Name the blood parasite species.
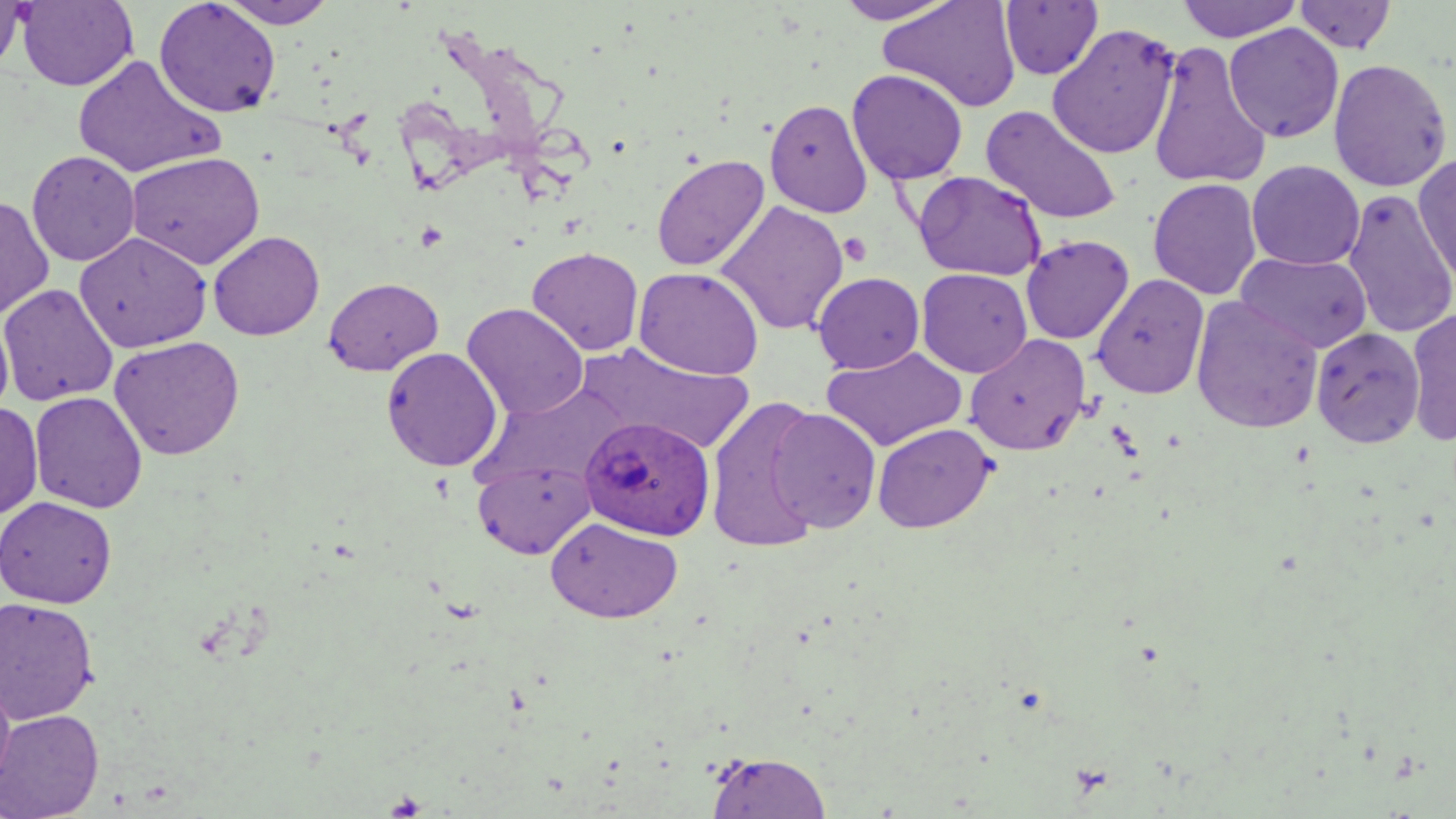
Plasmodium ovale.

Approximate bounding boxes as named x1/y1/x2/y2 corners in pixels. Platelet locations: (x1=415, y1=222, x2=448, y2=251), (x1=838, y1=233, x2=873, y2=266). Uninfected red blood cell locations: (x1=0, y1=0, x2=27, y2=76), (x1=16, y1=0, x2=138, y2=91), (x1=154, y1=0, x2=281, y2=118), (x1=217, y1=0, x2=338, y2=28), (x1=832, y1=0, x2=961, y2=25), (x1=879, y1=0, x2=1022, y2=112), (x1=1175, y1=0, x2=1304, y2=42), (x1=1000, y1=1, x2=1103, y2=80), (x1=1293, y1=1, x2=1398, y2=54), (x1=1046, y1=23, x2=1180, y2=160), (x1=1224, y1=23, x2=1344, y2=143), (x1=1149, y1=40, x2=1272, y2=191), (x1=72, y1=53, x2=225, y2=180), (x1=1328, y1=57, x2=1452, y2=192), (x1=847, y1=69, x2=968, y2=185), (x1=764, y1=99, x2=873, y2=218), (x1=980, y1=105, x2=1122, y2=226), (x1=26, y1=150, x2=141, y2=266), (x1=126, y1=151, x2=266, y2=270), (x1=1413, y1=152, x2=1456, y2=291), (x1=651, y1=153, x2=770, y2=272), (x1=1247, y1=160, x2=1365, y2=270), (x1=913, y1=170, x2=1046, y2=280), (x1=1147, y1=178, x2=1263, y2=301), (x1=1341, y1=189, x2=1456, y2=339), (x1=0, y1=195, x2=54, y2=320), (x1=716, y1=200, x2=849, y2=336), (x1=208, y1=230, x2=324, y2=341), (x1=74, y1=232, x2=212, y2=353), (x1=1020, y1=234, x2=1134, y2=345), (x1=527, y1=247, x2=644, y2=356), (x1=1236, y1=251, x2=1373, y2=354), (x1=634, y1=266, x2=764, y2=380), (x1=916, y1=268, x2=1032, y2=377), (x1=812, y1=272, x2=924, y2=374), (x1=1092, y1=273, x2=1209, y2=399), (x1=323, y1=277, x2=443, y2=376), (x1=0, y1=283, x2=118, y2=405), (x1=1190, y1=296, x2=1324, y2=434), (x1=462, y1=303, x2=588, y2=420), (x1=1404, y1=309, x2=1456, y2=446), (x1=0, y1=311, x2=14, y2=422), (x1=1312, y1=326, x2=1426, y2=448), (x1=965, y1=334, x2=1091, y2=455), (x1=108, y1=335, x2=245, y2=461), (x1=579, y1=343, x2=755, y2=454), (x1=821, y1=346, x2=968, y2=451), (x1=381, y1=347, x2=503, y2=471), (x1=29, y1=391, x2=147, y2=513), (x1=705, y1=395, x2=827, y2=553), (x1=0, y1=402, x2=43, y2=520), (x1=769, y1=407, x2=882, y2=533), (x1=872, y1=422, x2=996, y2=533), (x1=473, y1=460, x2=595, y2=558), (x1=0, y1=496, x2=117, y2=608), (x1=545, y1=517, x2=683, y2=623), (x1=0, y1=596, x2=100, y2=724), (x1=0, y1=672, x2=16, y2=796), (x1=0, y1=708, x2=104, y2=819), (x1=705, y1=751, x2=832, y2=819). Plasmodium ovale-infected red blood cell locations: (x1=579, y1=416, x2=715, y2=540). Light microscopy. Thin blood film. 1000x magnification. Image is 1456×819 pixels. Single field of view. May-Grünwald-Giemsa stain.